Report the malaria status of this cell.
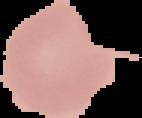

It is uninfected.

Summary:
  - Image type: segmented cell region with the area outside set to black
  - Preparation: thin blood film
  - Image size: 142×118 pixels